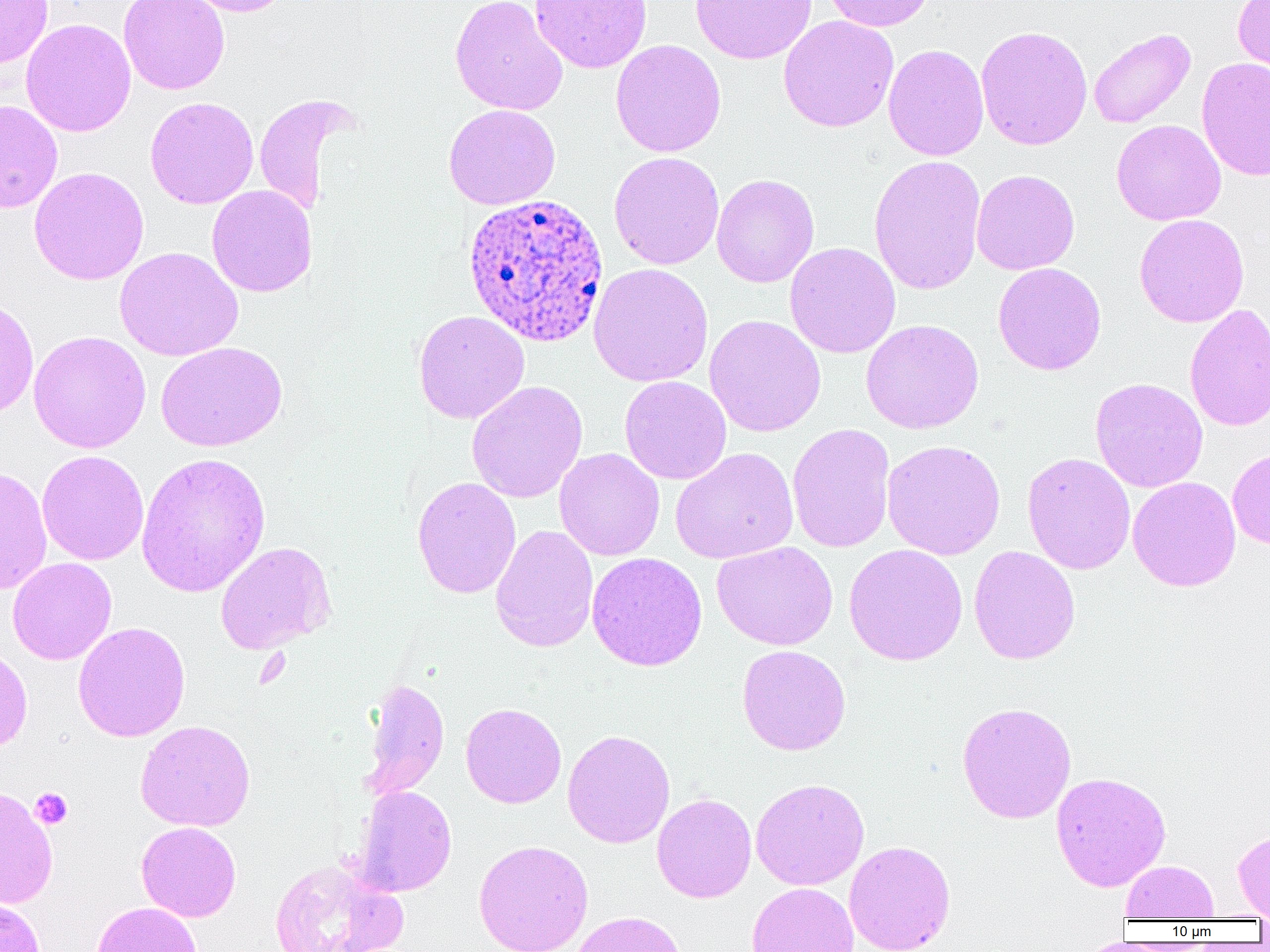
Summary:
  - Coordinate format: approximate bounding boxes as (x1, y1, x2, y2) in pixels
  - Uninfected red blood cell locations: (0, 0, 53, 68), (118, 0, 230, 95), (181, 0, 294, 17), (450, 0, 568, 116), (529, 0, 652, 73), (690, 0, 817, 64), (821, 0, 936, 32), (1232, 0, 1270, 80), (778, 15, 899, 132), (20, 18, 136, 137), (975, 24, 1093, 151), (1088, 28, 1196, 128), (610, 39, 726, 157), (883, 44, 989, 161), (1196, 57, 1270, 181), (252, 94, 358, 216), (145, 96, 259, 209), (0, 99, 63, 214), (444, 104, 560, 209), (1112, 119, 1226, 225), (609, 151, 725, 270), (868, 154, 986, 296), (28, 166, 150, 285), (971, 169, 1080, 275), (711, 174, 820, 288), (207, 185, 316, 297), (1134, 214, 1250, 328), (785, 242, 901, 359), (114, 247, 243, 361), (993, 262, 1106, 375), (588, 263, 713, 387), (0, 298, 39, 421), (1184, 303, 1270, 432), (413, 310, 530, 424), (704, 314, 826, 437), (860, 319, 984, 434), (28, 330, 151, 453), (155, 342, 287, 451), (619, 376, 732, 484), (1089, 377, 1208, 493), (466, 381, 588, 503), (787, 422, 895, 553), (882, 439, 1006, 560), (670, 447, 798, 564), (554, 448, 665, 561), (1227, 448, 1270, 549), (37, 450, 149, 565), (1022, 451, 1136, 575), (136, 452, 271, 598), (0, 466, 52, 595), (412, 476, 521, 599), (1128, 476, 1241, 591), (490, 524, 598, 653), (215, 541, 336, 654), (712, 541, 838, 650), (843, 543, 968, 666), (968, 545, 1081, 665), (586, 552, 707, 671), (7, 557, 117, 665), (72, 621, 190, 742), (737, 644, 851, 755), (0, 646, 33, 753), (362, 676, 449, 801), (956, 701, 1077, 824), (460, 702, 567, 808), (135, 720, 256, 832), (562, 729, 675, 849), (1050, 771, 1171, 891), (750, 778, 869, 890), (0, 784, 58, 910), (353, 785, 457, 897), (652, 793, 757, 903), (137, 822, 241, 922), (1233, 829, 1270, 920), (473, 839, 594, 952), (844, 840, 956, 952), (269, 859, 407, 952), (1121, 860, 1218, 921), (747, 882, 859, 952), (1, 897, 46, 952), (91, 901, 202, 952), (569, 911, 688, 952)
  - Platelet locations: (30, 788, 73, 829)
  - Plasmodium ovale-infected red blood cell locations: (460, 192, 610, 348)
  - Slide-level diagnosis: Plasmodium ovale
  - Field of view: single
  - Magnification: 1000x
  - Modality: light microscopy
  - Preparation: thin blood film
  - Image size: 1270×952 pixels